Report the malaria status of this cell.
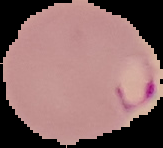
It is parasitized.

From a thin blood smear. Segmented cell region on a black background. Image is 163×148 pixels.